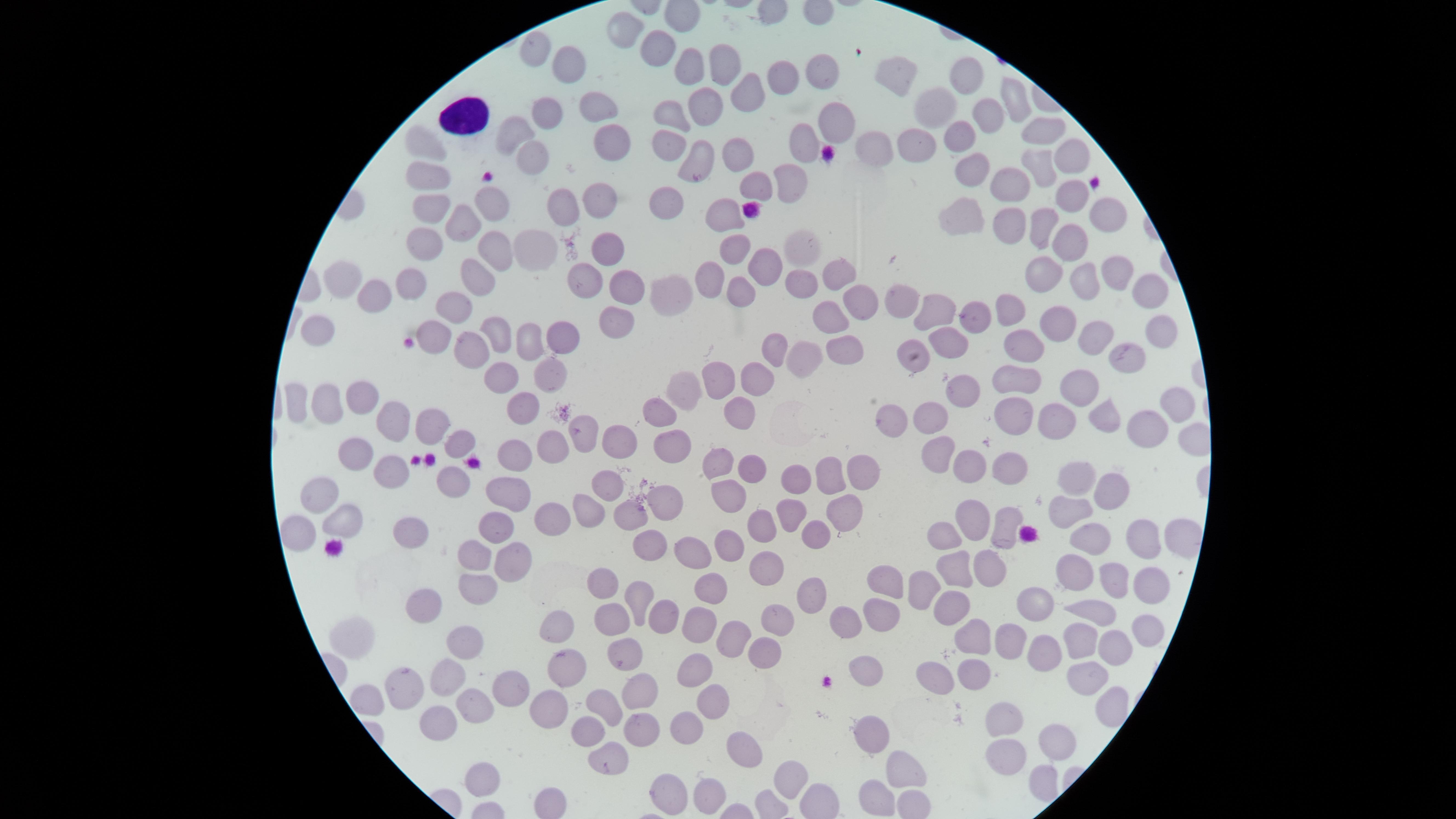

stain = Giemsa
image size = 1456×819 pixels
preparation = thin blood smear
presence = no malaria parasites identified
capture = smartphone photograph through the microscope eyepiece
field of view = single
white blood cells = approximate marker points, in pixels from the top-left corner: (x=467, y=117)
visible region = circular
uninfected red blood cells = approximate marker points, in pixels from the top-left corner: (x=624, y=28), (x=656, y=46), (x=526, y=51), (x=720, y=61), (x=689, y=65), (x=570, y=70), (x=816, y=72), (x=969, y=75), (x=783, y=76), (x=895, y=77), (x=744, y=98), (x=593, y=101), (x=1013, y=101), (x=699, y=104), (x=940, y=104), (x=543, y=114), (x=984, y=114), (x=831, y=118), (x=670, y=119), (x=509, y=136), (x=1040, y=136), (x=607, y=139), (x=957, y=139), (x=422, y=141), (x=802, y=144), (x=912, y=144), (x=668, y=150), (x=873, y=153), (x=735, y=155), (x=1069, y=155), (x=533, y=157), (x=697, y=158), (x=1039, y=167), (x=965, y=173), (x=428, y=175), (x=789, y=183), (x=1009, y=183), (x=1073, y=186), (x=598, y=196), (x=670, y=202), (x=554, y=207), (x=494, y=208), (x=426, y=210), (x=1110, y=212), (x=727, y=214), (x=1010, y=219), (x=1043, y=222), (x=464, y=224), (x=962, y=225), (x=1070, y=242), (x=426, y=244), (x=607, y=246), (x=737, y=246), (x=531, y=248), (x=501, y=251), (x=802, y=253), (x=767, y=259), (x=838, y=269), (x=1111, y=269), (x=1084, y=273), (x=475, y=274), (x=1047, y=274), (x=627, y=278), (x=336, y=279), (x=406, y=279), (x=582, y=281), (x=717, y=284), (x=803, y=286), (x=743, y=287), (x=678, y=293), (x=1150, y=293), (x=374, y=298), (x=904, y=303), (x=455, y=304), (x=862, y=304), (x=1009, y=307), (x=972, y=313), (x=939, y=315), (x=828, y=317), (x=617, y=320), (x=318, y=323), (x=1055, y=324), (x=436, y=332), (x=1157, y=332), (x=494, y=333), (x=560, y=335), (x=1092, y=335), (x=529, y=340), (x=944, y=340), (x=777, y=345), (x=471, y=346), (x=846, y=346), (x=1022, y=346), (x=913, y=354), (x=1121, y=356), (x=799, y=359), (x=553, y=370), (x=504, y=374), (x=1022, y=375), (x=761, y=379), (x=719, y=381), (x=1080, y=384), (x=959, y=389), (x=678, y=390), (x=287, y=398), (x=359, y=398), (x=520, y=403), (x=1174, y=403), (x=325, y=404), (x=663, y=409), (x=393, y=415), (x=1014, y=415), (x=1102, y=416), (x=738, y=418), (x=929, y=419), (x=892, y=420), (x=1062, y=422), (x=435, y=426), (x=582, y=429), (x=1143, y=432), (x=459, y=440), (x=545, y=443), (x=614, y=443), (x=669, y=447), (x=512, y=451), (x=933, y=454), (x=352, y=458), (x=714, y=463), (x=749, y=463), (x=1011, y=464), (x=390, y=467), (x=964, y=467), (x=831, y=472), (x=861, y=473), (x=1084, y=478), (x=792, y=482), (x=451, y=483), (x=608, y=486), (x=508, y=489), (x=312, y=492), (x=728, y=494), (x=1110, y=496), (x=666, y=502), (x=841, y=507), (x=587, y=511), (x=790, y=514), (x=1064, y=515), (x=633, y=516), (x=977, y=516), (x=342, y=521), (x=1006, y=525), (x=496, y=526), (x=410, y=527), (x=547, y=528), (x=755, y=533), (x=1175, y=538), (x=731, y=541), (x=947, y=541), (x=1146, y=541), (x=293, y=543), (x=646, y=543), (x=809, y=543), (x=1087, y=544), (x=691, y=552), (x=469, y=557), (x=508, y=560), (x=986, y=567), (x=765, y=568), (x=951, y=570), (x=1075, y=571), (x=1107, y=577), (x=1142, y=581), (x=883, y=584), (x=711, y=585), (x=920, y=587), (x=603, y=588), (x=806, y=592), (x=475, y=596), (x=636, y=600), (x=948, y=603), (x=1037, y=604), (x=431, y=605), (x=1091, y=607), (x=656, y=613), (x=773, y=616), (x=843, y=619), (x=877, y=619), (x=611, y=623), (x=693, y=625), (x=558, y=630), (x=1136, y=630), (x=731, y=631), (x=969, y=636), (x=353, y=639), (x=1076, y=639), (x=1006, y=643), (x=464, y=649), (x=1111, y=649), (x=1045, y=650), (x=762, y=652), (x=626, y=655), (x=862, y=663), (x=566, y=668), (x=691, y=668), (x=978, y=669), (x=1083, y=675), (x=938, y=678), (x=439, y=683), (x=396, y=688), (x=634, y=692), (x=507, y=695), (x=362, y=698), (x=706, y=701), (x=601, y=702), (x=476, y=707), (x=1105, y=707), (x=542, y=709), (x=1005, y=713), (x=440, y=720), (x=687, y=725), (x=589, y=732), (x=866, y=732), (x=641, y=737), (x=1048, y=742), (x=742, y=747), (x=1005, y=757), (x=608, y=763), (x=901, y=772), (x=792, y=773), (x=480, y=777), (x=662, y=789), (x=700, y=791), (x=879, y=796)